State which cell type is depicted.
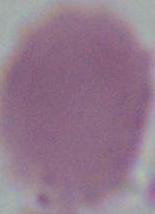

This is an erythrocyte.

Photomicrograph. Captured at 1000x magnification.